Classify this cell by malaria status.
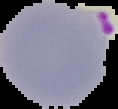
It is parasitized.

image type = segmented cell region with the area outside set to black
image size = 118×109 pixels
preparation = thin blood smear